Assess this cell for malaria.
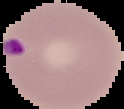
It is parasitized.

Summary:
  - Image size: 124×109 pixels
  - Preparation: thin blood smear
  - Image type: segmented cell region with the area outside set to black